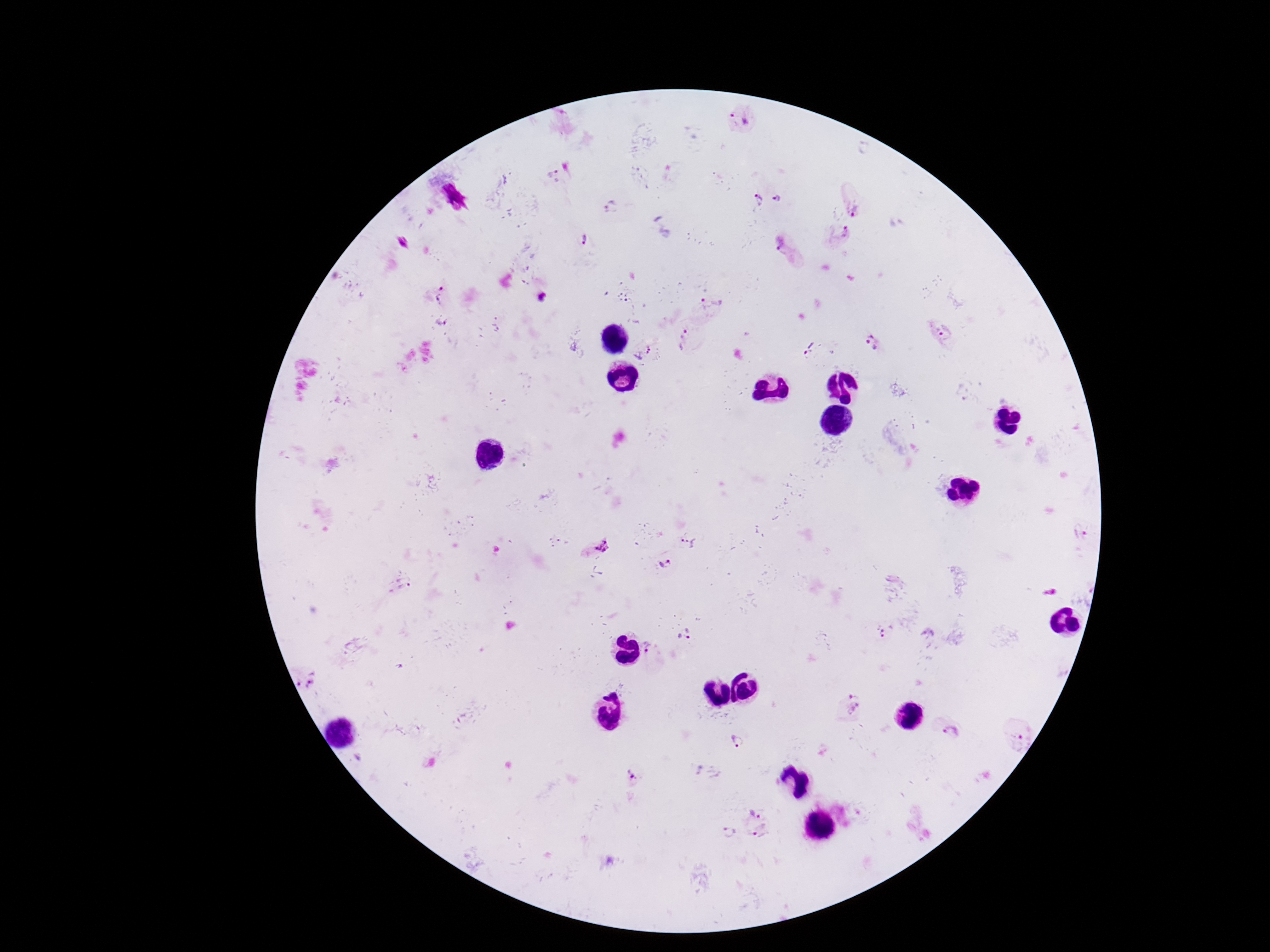

Approximate object centers, in pixels from the top-left corner.
Summary:
  - Plasmodium parasite locations: (x=740, y=118), (x=552, y=171), (x=758, y=199), (x=779, y=200), (x=612, y=207), (x=854, y=207), (x=840, y=233), (x=585, y=240), (x=785, y=248), (x=438, y=294), (x=542, y=298), (x=947, y=329), (x=684, y=338), (x=873, y=342), (x=640, y=352), (x=808, y=354), (x=1081, y=533), (x=687, y=542), (x=595, y=544), (x=667, y=564), (x=399, y=585), (x=687, y=634), (x=887, y=634), (x=650, y=650), (x=306, y=677), (x=854, y=703), (x=951, y=732), (x=1020, y=735), (x=739, y=743), (x=634, y=777), (x=755, y=810), (x=729, y=832), (x=762, y=833)
  - Field of view: one from this slide
  - Image size: 1270×952 pixels
  - Patient malaria status: infected
  - Magnification: 100x
  - Stain: Giemsa
  - Capture: smartphone camera through the microscope eyepiece
  - Preparation: thick blood film